Classify this cell by malaria status.
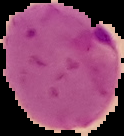

It is parasitized.

Summary:
  - Preparation: thin blood film
  - Image type: segmented cell region with the area outside set to black
  - Image size: 124×136 pixels